Give the position of every Plasmodium parasite.
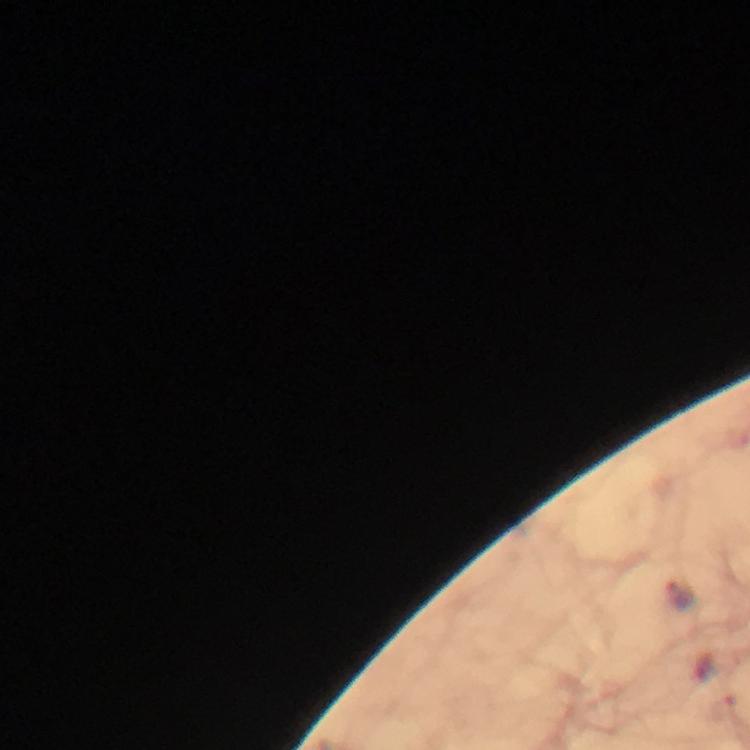
Approximate centers as [x, y] in pixels.
Plasmodium parasites: [681, 594].

Image is 750×750 pixels. From a malaria diagnostic workup. Immersion oil was used. Cropped region of a single field of view. Thick blood smear. Photographed through the microscope with a smartphone camera. 100x magnification. Giemsa-stained preparation.